Comment on the morphology of the erythrocytes.
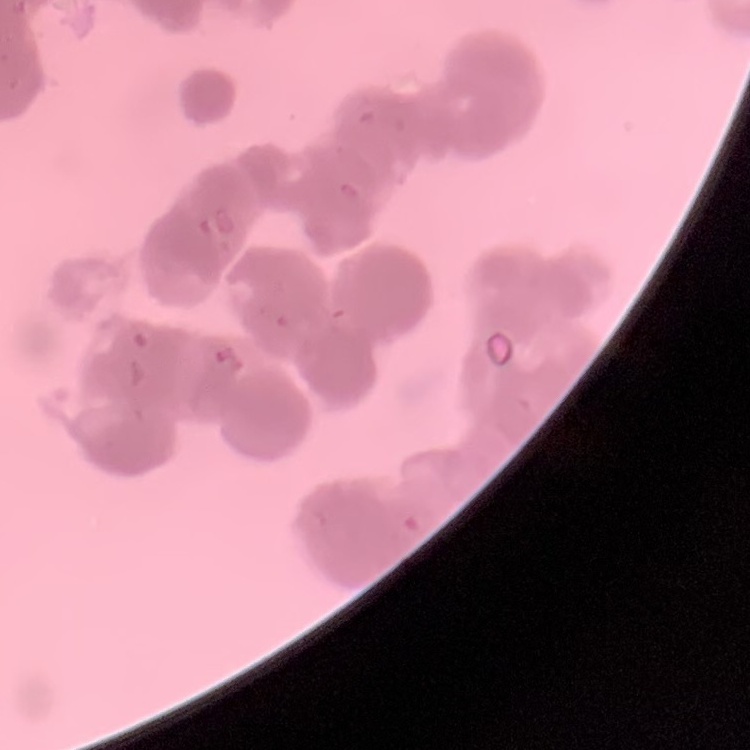

They show rouleaux formation.

Thin peripheral smear. Square crop of a larger photomicrograph. Stained with either Field's or Giemsa.